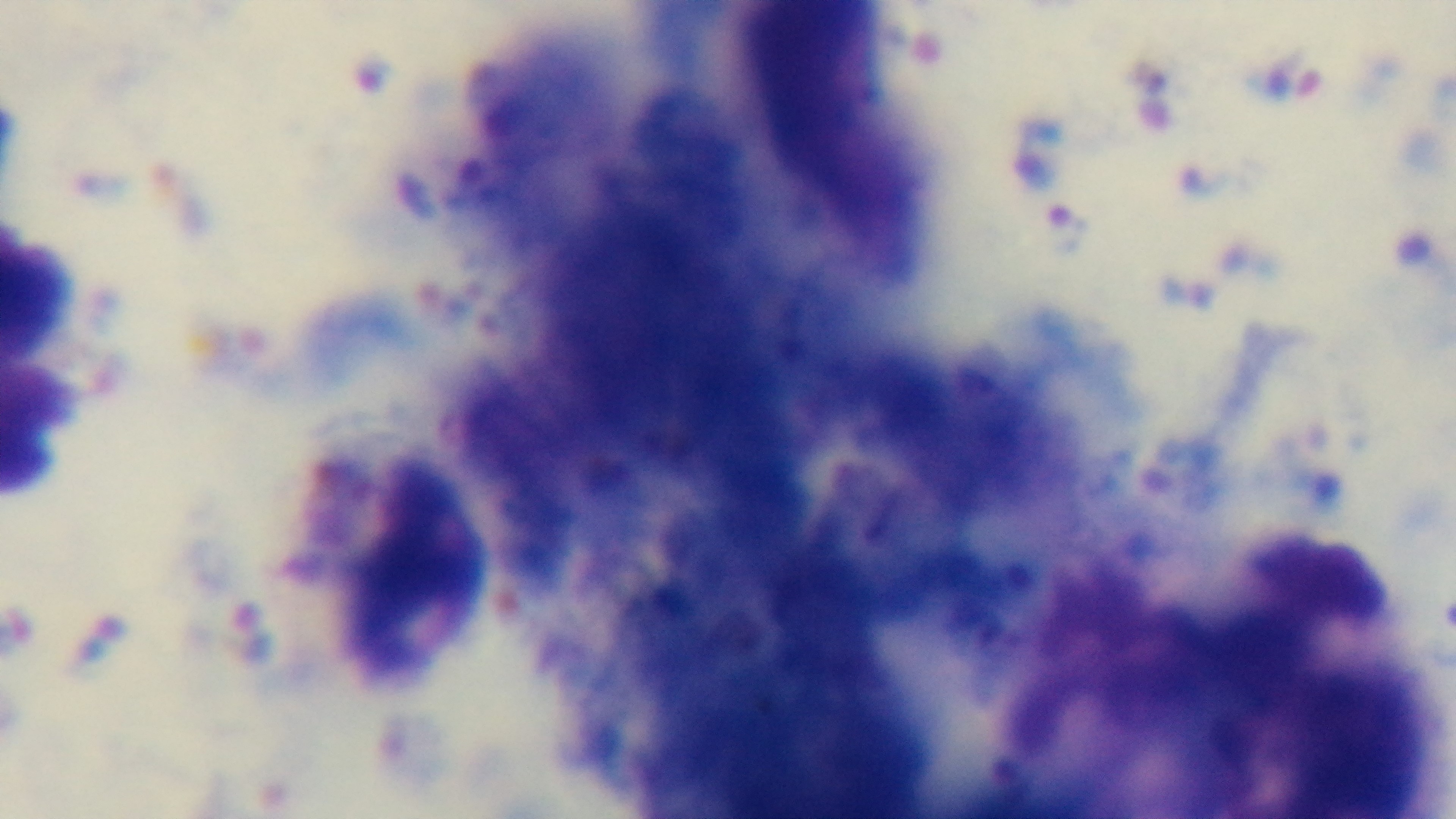
malaria status = infected
objective = 100x oil immersion
capture = mounted 4K digital camera
preparation = thick blood film
modality = light microscopy
stain = Giemsa
field of view = one from the slide